State which parasite is depicted.
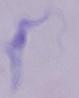
A trypanosome.

Summary:
  - Magnification: 1000x
  - Modality: micrograph